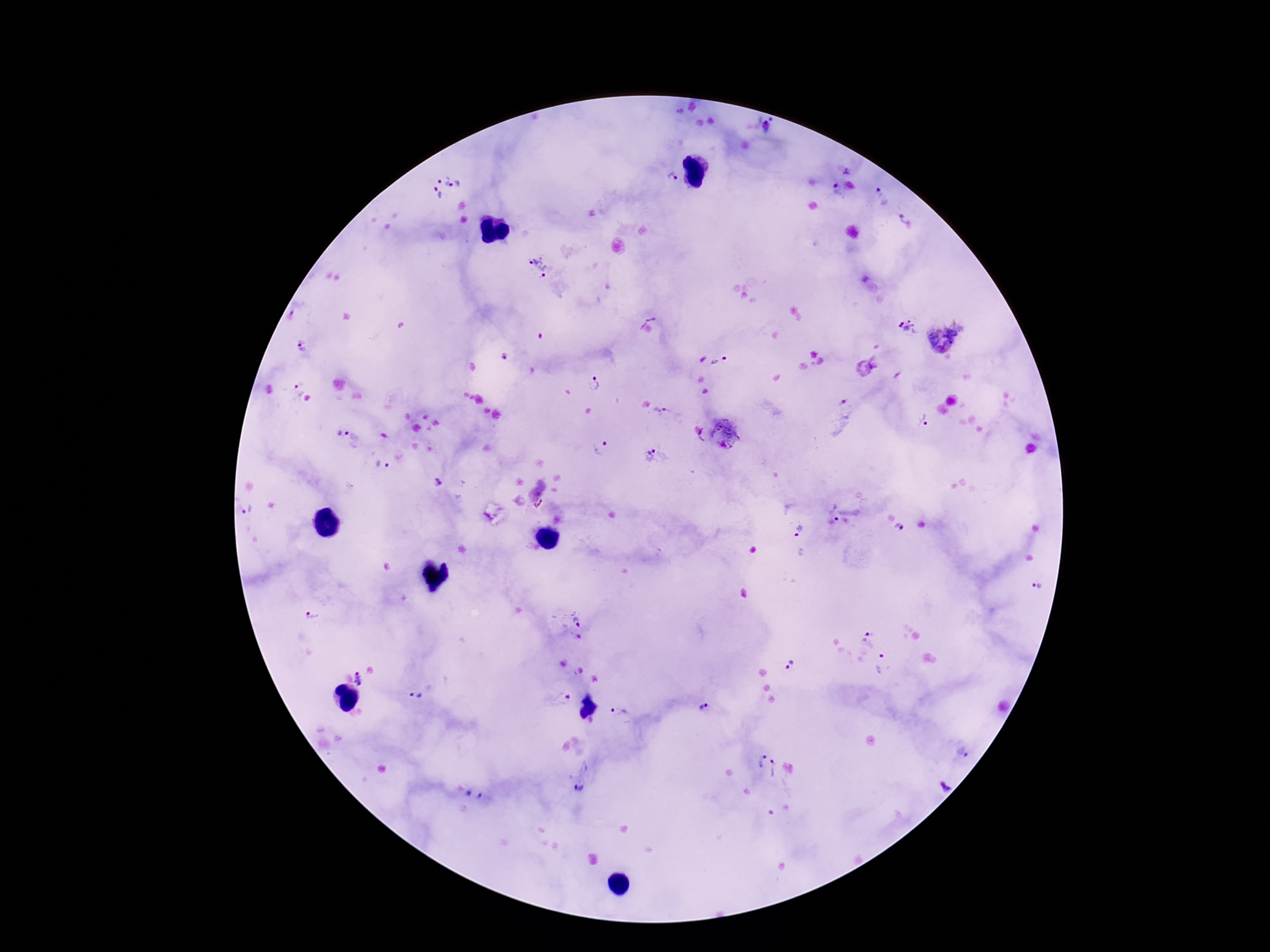 Approximate centers as (x, y) in pixels. Plasmodium parasite locations: (771, 119), (767, 128), (847, 172), (672, 177), (443, 180), (456, 185), (835, 185), (438, 194), (882, 196), (905, 218), (534, 258), (548, 271), (298, 307), (908, 328), (945, 335), (303, 348), (505, 356), (719, 361), (595, 383), (298, 390), (662, 411), (843, 416), (924, 421), (726, 432), (344, 434), (599, 449), (652, 456), (383, 466), (438, 482), (246, 510), (835, 512), (900, 528), (798, 530), (1037, 586), (311, 618), (576, 621), (862, 634), (883, 665), (789, 666), (360, 680), (415, 696), (558, 698), (701, 709), (618, 711), (963, 753), (757, 759), (776, 769), (943, 786), (579, 789), (474, 797). Image is 1270×952 pixels. 100x magnification. Photographed through the microscope eyepiece with a smartphone camera. One field from this slide. Thick peripheral-blood smear. Giemsa stain. Patient malaria status: infected.